Report the malaria status of this cell.
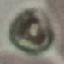
Uninfected.

image type = cell patch, automatically extracted from a larger field of view and resized to 64 × 64 pixels
stain = Giemsa
capture = smartphone camera at the microscope eyepiece
preparation = thin blood smear